Locate every malaria parasite.
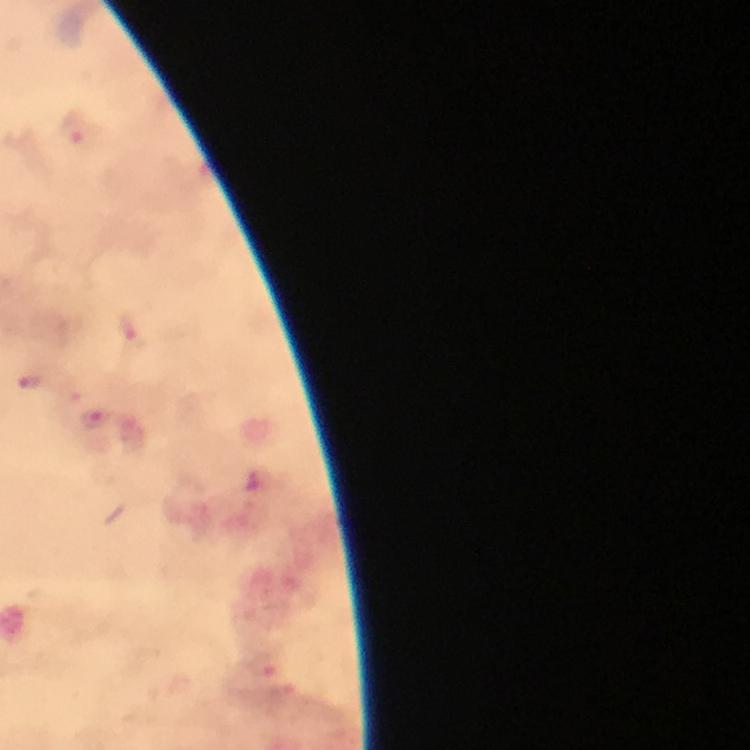

Approximate centers as {x, y} in pixels.
Malaria parasites: {77, 134}, {133, 335}, {33, 380}, {95, 422}.

Summary:
  - Cropped from: a single field of view
  - Image size: 750×750 pixels
  - Magnification: 100x
  - Preparation: thick blood smear
  - Capture: smartphone photograph through a microscope
  - Stain: Giemsa
  - Context: from a diagnostic examination for malaria
  - Immersion oil: used